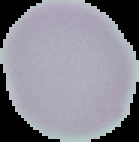 Segmented cell region on a black background. Result: no Plasmodium parasites detected. From a thin blood smear. Image is 139×142 pixels.